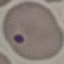
Summary:
  - Result: malaria parasites identified
  - Preparation: thin blood film
  - Capture: smartphone through the microscope eyepiece
  - Stain: Giemsa
  - Image type: automatically extracted cell patch, resized to 64 × 64 pixels